Identify the blood parasite species.
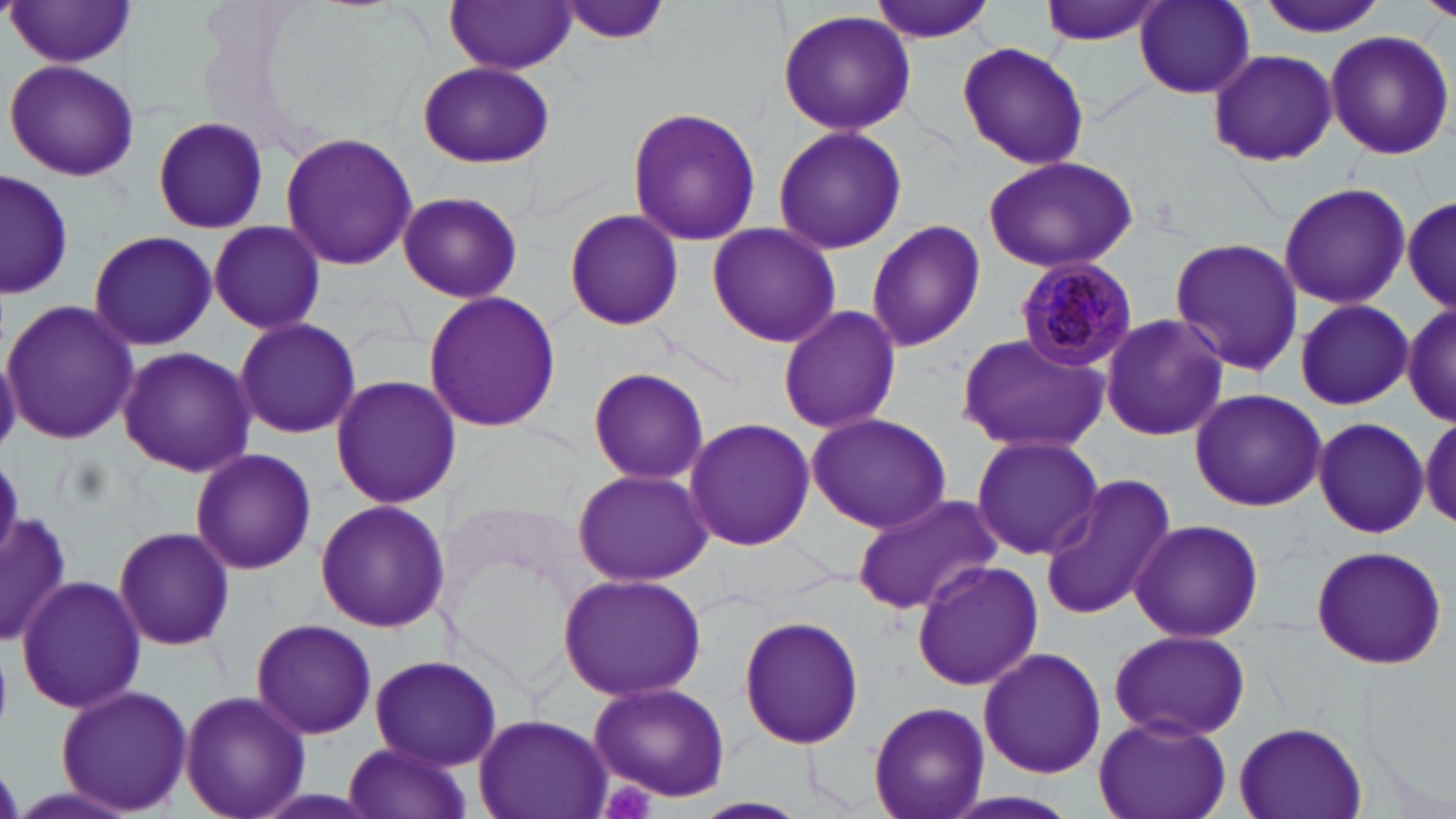
Plasmodium malariae.

{
  "platelet_locations": "approximate bounding boxes as named x1/y1/x2/y2 corners in pixels: (x1=598, y1=779, x2=656, y2=819)",
  "preparation": "thin blood film",
  "uninfected_red_blood_cell_locations": "approximate bounding boxes as named x1/y1/x2/y2 corners in pixels: (x1=554, y1=0, x2=672, y2=48), (x1=866, y1=0, x2=997, y2=43), (x1=1040, y1=0, x2=1168, y2=46), (x1=1131, y1=0, x2=1259, y2=100), (x1=1256, y1=0, x2=1388, y2=40), (x1=6, y1=1, x2=137, y2=69), (x1=446, y1=1, x2=575, y2=74), (x1=776, y1=9, x2=917, y2=137), (x1=1324, y1=30, x2=1455, y2=159), (x1=956, y1=42, x2=1090, y2=171), (x1=1207, y1=49, x2=1337, y2=164), (x1=5, y1=60, x2=141, y2=181), (x1=416, y1=60, x2=554, y2=169), (x1=626, y1=107, x2=762, y2=248), (x1=148, y1=115, x2=272, y2=234), (x1=770, y1=125, x2=910, y2=256), (x1=279, y1=131, x2=417, y2=272), (x1=981, y1=155, x2=1138, y2=274), (x1=0, y1=169, x2=74, y2=304), (x1=1278, y1=181, x2=1410, y2=310), (x1=397, y1=190, x2=523, y2=304), (x1=1402, y1=194, x2=1454, y2=315), (x1=564, y1=207, x2=685, y2=332), (x1=865, y1=219, x2=986, y2=353), (x1=206, y1=220, x2=327, y2=336), (x1=705, y1=224, x2=842, y2=348), (x1=87, y1=229, x2=217, y2=352), (x1=1169, y1=236, x2=1304, y2=377), (x1=421, y1=290, x2=562, y2=435), (x1=2, y1=299, x2=140, y2=446), (x1=1293, y1=299, x2=1412, y2=411), (x1=1403, y1=299, x2=1455, y2=426), (x1=777, y1=305, x2=903, y2=436), (x1=1096, y1=313, x2=1229, y2=443), (x1=232, y1=317, x2=363, y2=440), (x1=955, y1=332, x2=1109, y2=454), (x1=0, y1=341, x2=22, y2=454), (x1=117, y1=346, x2=259, y2=477), (x1=584, y1=364, x2=711, y2=486), (x1=327, y1=375, x2=461, y2=510), (x1=1189, y1=388, x2=1327, y2=512), (x1=805, y1=412, x2=953, y2=534), (x1=1421, y1=412, x2=1456, y2=530), (x1=1312, y1=415, x2=1429, y2=539), (x1=682, y1=417, x2=814, y2=551), (x1=971, y1=434, x2=1103, y2=560), (x1=190, y1=448, x2=318, y2=576), (x1=569, y1=467, x2=714, y2=585), (x1=1038, y1=474, x2=1175, y2=622), (x1=849, y1=492, x2=1005, y2=615), (x1=314, y1=499, x2=449, y2=634), (x1=0, y1=509, x2=73, y2=648), (x1=1127, y1=518, x2=1264, y2=643), (x1=113, y1=525, x2=235, y2=651), (x1=1309, y1=544, x2=1450, y2=669), (x1=911, y1=560, x2=1043, y2=693), (x1=556, y1=571, x2=707, y2=701), (x1=17, y1=574, x2=147, y2=714), (x1=738, y1=615, x2=866, y2=750), (x1=250, y1=617, x2=377, y2=740), (x1=1109, y1=629, x2=1250, y2=741), (x1=978, y1=645, x2=1106, y2=779), (x1=368, y1=654, x2=503, y2=770), (x1=587, y1=679, x2=732, y2=804), (x1=55, y1=683, x2=193, y2=815), (x1=179, y1=689, x2=309, y2=819), (x1=866, y1=702, x2=989, y2=819), (x1=473, y1=714, x2=611, y2=818), (x1=1091, y1=715, x2=1232, y2=819), (x1=1234, y1=722, x2=1366, y2=819), (x1=340, y1=742, x2=472, y2=819), (x1=937, y1=791, x2=1086, y2=819)",
  "field_of_view": "single",
  "stain": "May-Grünwald-Giemsa",
  "plasmodium_malariae_infected_red_blood_cell_locations": "approximate bounding boxes as named x1/y1/x2/y2 corners in pixels: (x1=1012, y1=257, x2=1136, y2=372)",
  "magnification": "1000x",
  "image_size": "1456×819 pixels",
  "modality": "optical microscopy"
}